Outline each blood parasite and name the species.
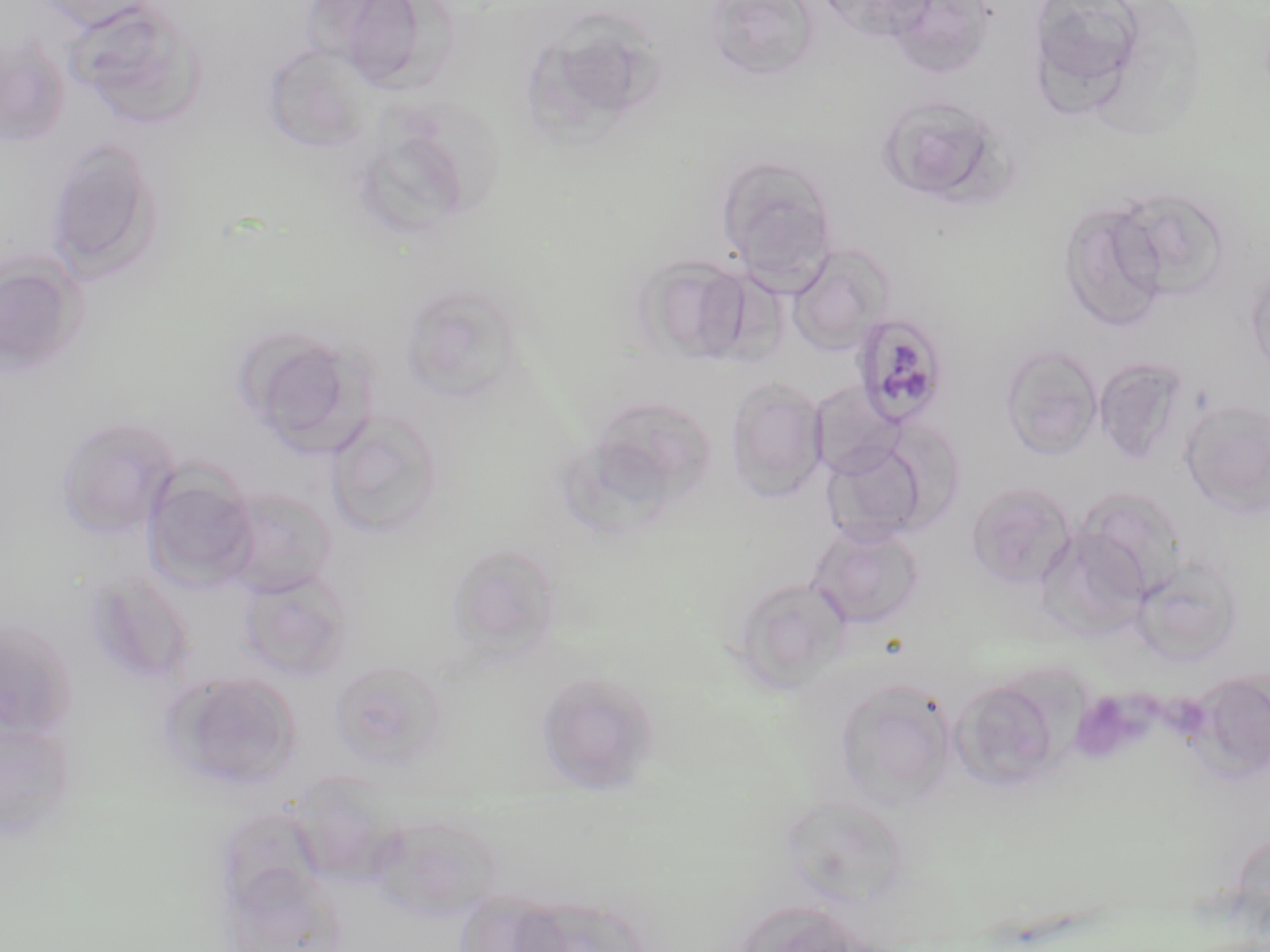

Approximate bounding boxes as named x1/y1/x2/y2 corners in pixels.
Plasmodium malariae-infected red blood cells: (x1=850, y1=311, x2=951, y2=428).
No Plasmodium falciparum, Plasmodium ovale, Plasmodium vivax, Babesia divergens, or Trypanosoma brucei observed.

slide-level diagnosis = Plasmodium malariae
stain = May-Grünwald-Giemsa
image size = 1270×952 pixels
preparation = thin blood film
field of view = one of a larger specimen
uninfected red blood cell locations = approximate bounding boxes as named x1/y1/x2/y2 corners in pixels: (x1=32, y1=0, x2=160, y2=32), (x1=705, y1=0, x2=820, y2=82), (x1=817, y1=0, x2=938, y2=42), (x1=881, y1=0, x2=997, y2=71), (x1=68, y1=1, x2=209, y2=130), (x1=306, y1=2, x2=426, y2=78), (x1=352, y1=2, x2=467, y2=91), (x1=1034, y1=3, x2=1153, y2=88), (x1=554, y1=14, x2=678, y2=120), (x1=0, y1=36, x2=70, y2=149), (x1=262, y1=43, x2=374, y2=153), (x1=875, y1=94, x2=1015, y2=210), (x1=44, y1=139, x2=164, y2=284), (x1=358, y1=140, x2=477, y2=246), (x1=716, y1=154, x2=839, y2=282), (x1=1112, y1=186, x2=1232, y2=304), (x1=1057, y1=201, x2=1170, y2=331), (x1=788, y1=245, x2=893, y2=355), (x1=0, y1=253, x2=87, y2=380), (x1=635, y1=253, x2=754, y2=365), (x1=1245, y1=263, x2=1270, y2=381), (x1=399, y1=280, x2=527, y2=405), (x1=235, y1=325, x2=368, y2=452), (x1=1000, y1=344, x2=1103, y2=460), (x1=1095, y1=357, x2=1191, y2=466), (x1=726, y1=377, x2=828, y2=502), (x1=809, y1=382, x2=903, y2=478), (x1=571, y1=394, x2=721, y2=527), (x1=1180, y1=399, x2=1270, y2=519), (x1=325, y1=409, x2=443, y2=540), (x1=54, y1=415, x2=180, y2=539), (x1=822, y1=441, x2=931, y2=547), (x1=142, y1=469, x2=260, y2=592), (x1=966, y1=482, x2=1077, y2=589), (x1=221, y1=487, x2=336, y2=597), (x1=1076, y1=487, x2=1189, y2=598), (x1=808, y1=523, x2=925, y2=630), (x1=1035, y1=525, x2=1150, y2=639), (x1=447, y1=543, x2=562, y2=663), (x1=1132, y1=557, x2=1244, y2=666), (x1=239, y1=570, x2=354, y2=682), (x1=83, y1=571, x2=195, y2=687), (x1=734, y1=577, x2=854, y2=688), (x1=0, y1=616, x2=78, y2=742), (x1=328, y1=658, x2=448, y2=770), (x1=1191, y1=669, x2=1270, y2=783), (x1=164, y1=671, x2=303, y2=792), (x1=534, y1=671, x2=662, y2=792), (x1=948, y1=674, x2=1076, y2=793), (x1=832, y1=678, x2=957, y2=807), (x1=1, y1=720, x2=76, y2=843), (x1=777, y1=792, x2=913, y2=909), (x1=370, y1=814, x2=502, y2=920), (x1=732, y1=900, x2=873, y2=952)
magnification = 1000x
modality = light microscopy